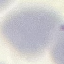 Result: no malaria parasites seen. Acquired by smartphone through the microscope eyepiece. Cell patch, automatically extracted from a larger field of view and resized to 64 × 64 pixels. Giemsa stain. Thin blood film.